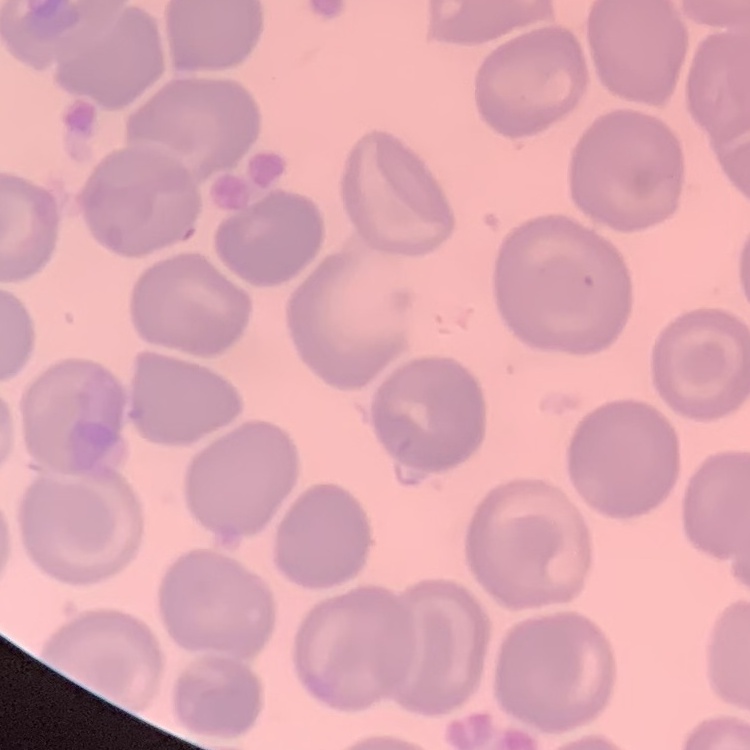
Summary:
  - Erythrocyte morphology: no rouleaux formation
  - Stain: Field's or Giemsa
  - Preparation: thin blood smear
  - Image type: square crop of a larger photomicrograph